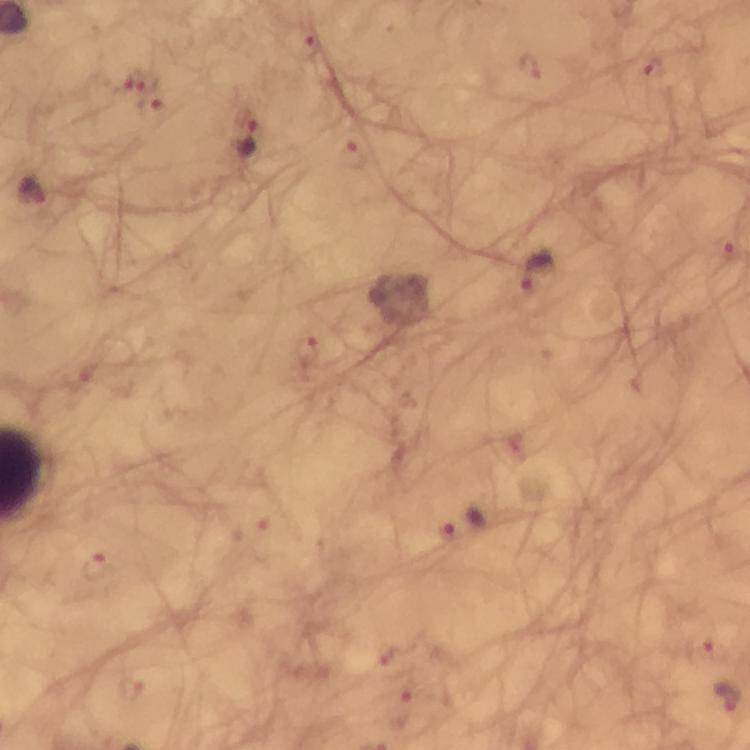
Approximate centers as {x, y} in pixels.
Summary:
  - Plasmodium parasite locations: {309, 44}, {652, 66}, {529, 68}, {138, 79}, {150, 105}, {249, 141}, {350, 155}, {33, 192}, {730, 251}, {537, 273}, {308, 351}, {251, 529}, {447, 531}, {96, 567}, {696, 648}, {389, 655}, {133, 687}, {402, 710}
  - Preparation: thick blood smear
  - Cropped from: a single field of view
  - Stain: Giemsa
  - Magnification: 100x
  - Immersion oil: applied
  - Context: from a diagnostic examination for malaria
  - Capture: smartphone mounted on the microscope
  - Image size: 750×750 pixels